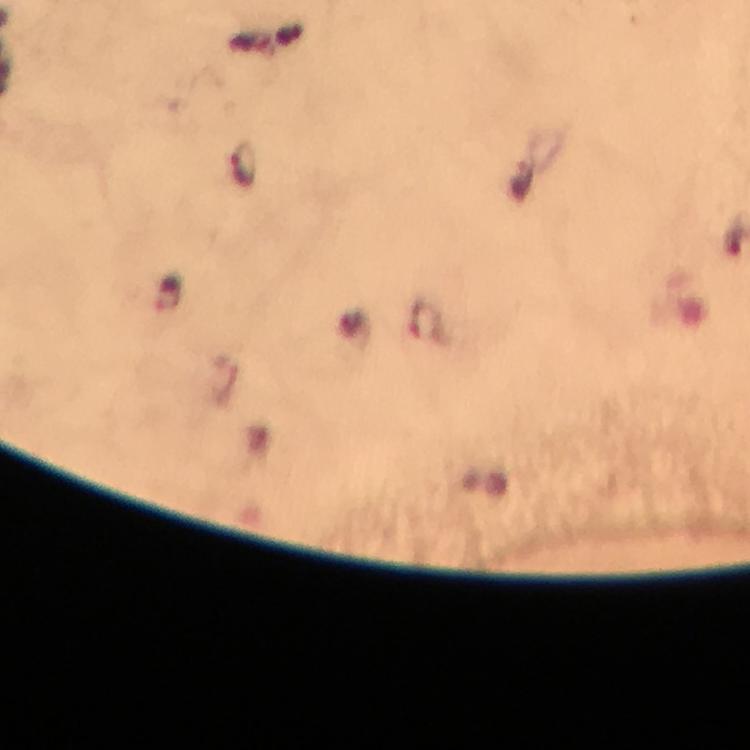

Approximate centers as {x, y} in pixels.
Summary:
  - Plasmodium parasite locations: {244, 164}, {169, 297}
  - Capture: smartphone mounted on the microscope
  - Preparation: thick blood film
  - Magnification: 100x
  - Image size: 750×750 pixels
  - Cropped from: one field of view
  - Context: from a diagnostic examination for malaria
  - Stain: Giemsa
  - Immersion oil: used